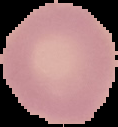
Summary:
  - Malaria status: uninfected
  - Image type: segmented cell region on a black background
  - Image size: 118×127 pixels
  - Preparation: thin blood film